Locate platelets.
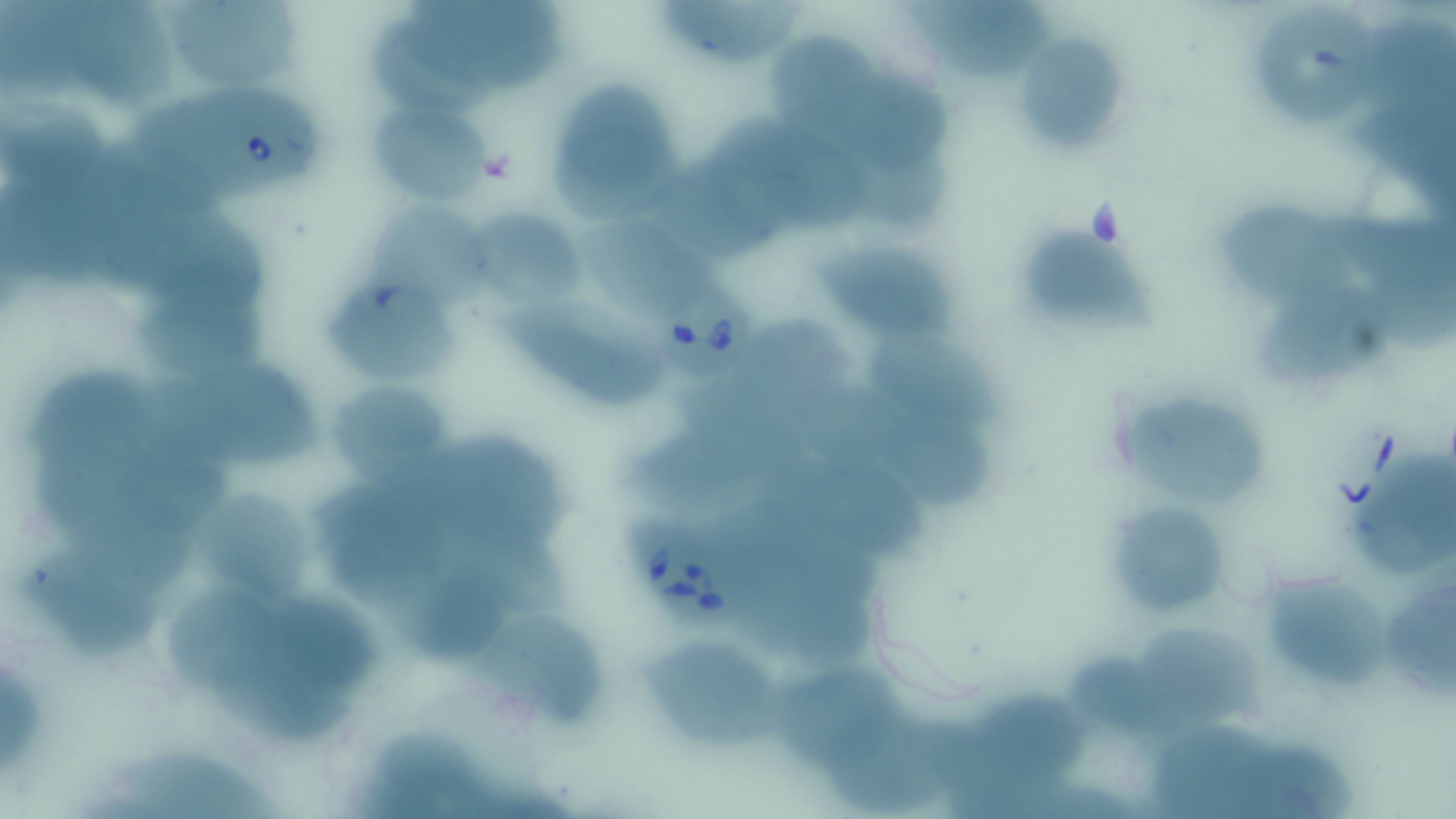

Approximate bounding boxes as (x1, y1, x2, y2) in pixels.
Platelets: (478, 150, 516, 184).

slide-level diagnosis = Babesia divergens
preparation = thin blood smear
image size = 1456×819 pixels
stain = May-Grünwald-Giemsa
Babesia divergens-infected red blood cell locations = approximate bounding boxes as (x1, y1, x2, y2) in pixels: (204, 83, 326, 189), (642, 270, 761, 381), (626, 513, 744, 629)
uninfected red blood cell locations = approximate bounding boxes as (x1, y1, x2, y2) in pixels: (67, 0, 171, 105), (413, 0, 565, 91), (660, 0, 812, 67), (897, 0, 1068, 81), (165, 2, 303, 90), (1255, 7, 1379, 131), (1352, 18, 1456, 117), (371, 20, 502, 115), (1012, 29, 1132, 158), (768, 30, 883, 141), (825, 72, 957, 176), (545, 77, 683, 212), (133, 97, 246, 200), (1351, 97, 1456, 203), (1, 99, 112, 183), (373, 102, 492, 205), (711, 114, 843, 194), (848, 147, 959, 229), (647, 159, 795, 261), (1220, 200, 1364, 304), (370, 202, 495, 307), (472, 202, 587, 312), (1332, 208, 1456, 280), (565, 210, 722, 319), (112, 215, 276, 312), (1006, 215, 1157, 347), (811, 227, 963, 347), (1363, 269, 1456, 353), (322, 280, 464, 382), (1257, 284, 1397, 387), (141, 289, 283, 384), (500, 295, 673, 402), (734, 316, 850, 397), (865, 325, 1004, 429), (143, 363, 330, 474), (30, 370, 164, 473), (325, 375, 458, 485), (680, 378, 817, 450), (1125, 392, 1269, 512), (870, 399, 1000, 517), (418, 430, 574, 556), (628, 430, 764, 516), (1349, 448, 1456, 580), (755, 454, 927, 557), (128, 457, 238, 536), (192, 480, 321, 611), (76, 488, 207, 596), (1116, 498, 1223, 610), (330, 503, 456, 604), (432, 523, 569, 618), (21, 546, 163, 658), (743, 570, 881, 670), (1262, 571, 1395, 698), (389, 574, 508, 658), (1386, 574, 1456, 701), (164, 587, 287, 691), (274, 592, 386, 692), (468, 609, 614, 722), (1144, 618, 1259, 721), (1071, 637, 1200, 748), (643, 645, 804, 754), (214, 654, 366, 743), (0, 663, 44, 777), (771, 663, 904, 769), (975, 683, 1090, 781), (831, 714, 961, 815), (1148, 724, 1286, 819), (381, 726, 494, 819), (118, 746, 279, 819), (1236, 746, 1362, 819)
magnification = 1000x
field of view = single
modality = light microscopy